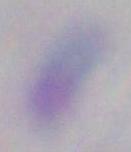
Summary:
  - Modality: photomicrograph
  - Magnification: 1000x
  - Identification: Toxoplasma gondii